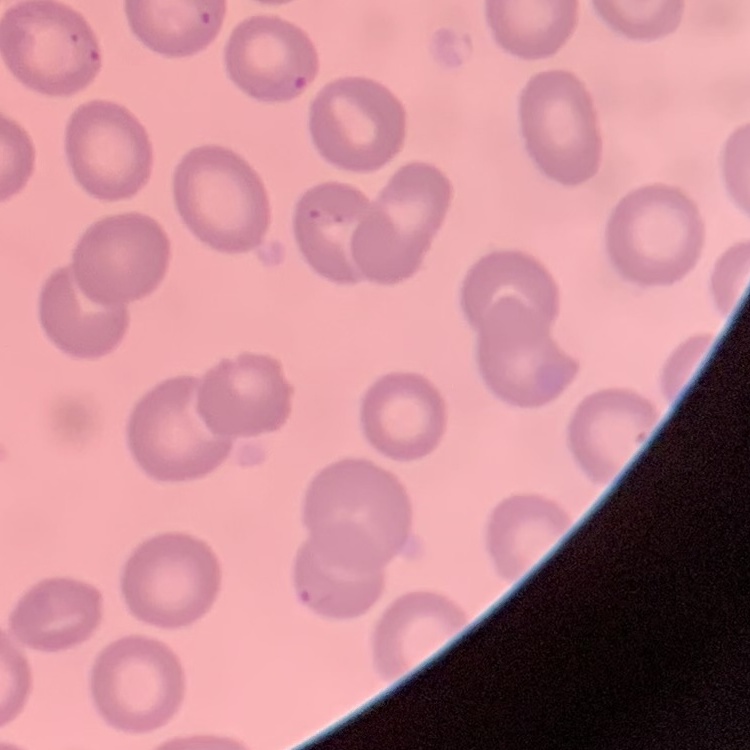

The erythrocytes show no rouleaux formation. One tile cut from a larger photomicrograph. Stained with either Field's or Giemsa. Thin blood film.